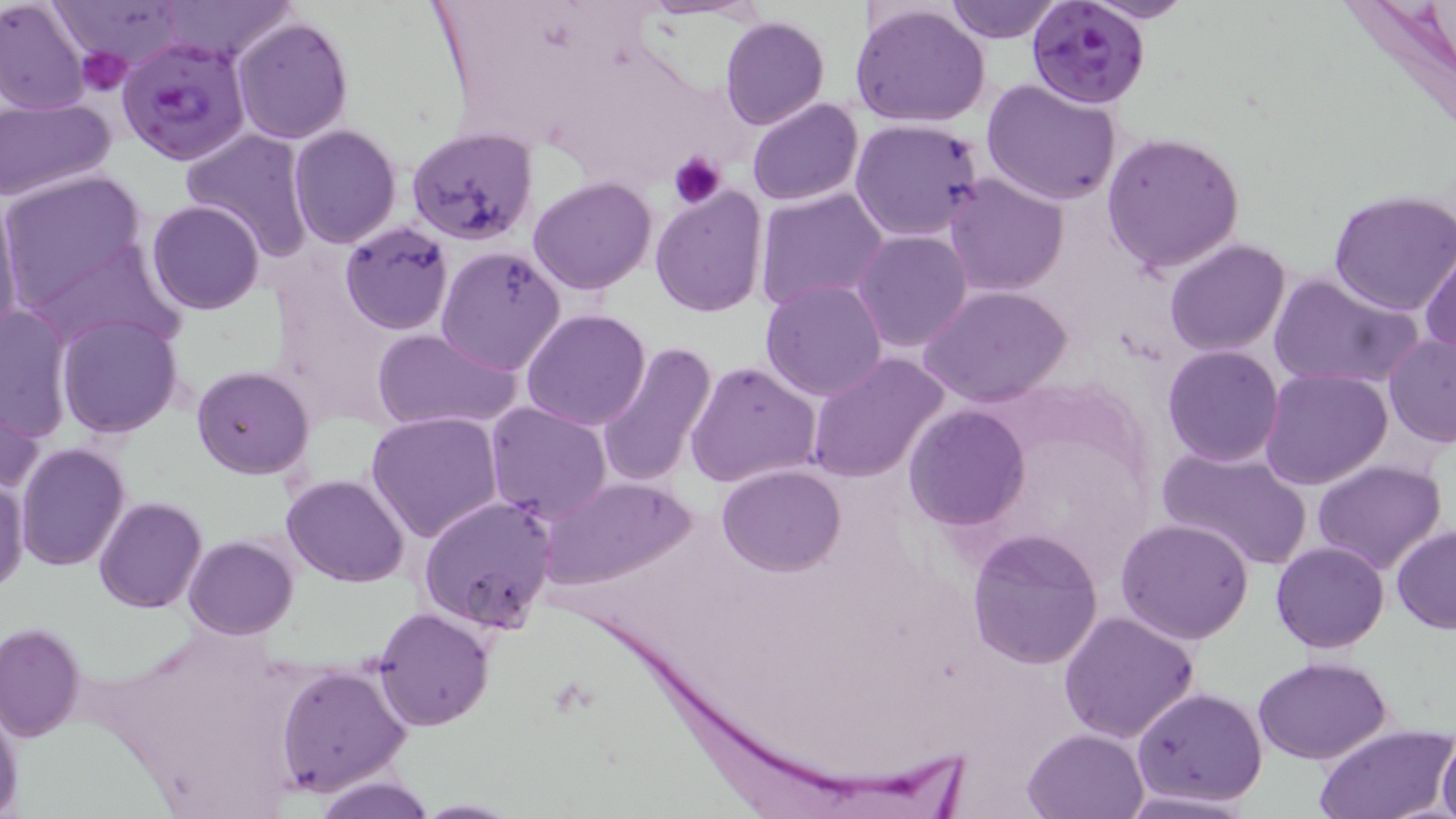
slide-level diagnosis = Plasmodium falciparum
field of view = one of a larger specimen
preparation = thin blood smear
platelet locations = approximate bounding boxes as (x1,y1)-(x2,y2) corner pairs in pixels: (77,45)-(131,94), (668,152)-(726,207)
image size = 1456×819 pixels
modality = light microscopy
Plasmodium falciparum-infected red blood cell locations = approximate bounding boxes as (x1,y1)-(x2,y2) corner pairs in pixels: (1027,0)-(1152,109), (115,37)-(252,164)
uninfected red blood cell locations = approximate bounding boxes as (x1,y1)-(x2,y2) corner pairs in pixels: (52,0)-(191,64), (157,0)-(299,65), (945,0)-(1063,43), (1085,0)-(1195,23), (0,1)-(90,116), (849,4)-(992,130), (231,15)-(353,144), (720,15)-(828,129), (981,78)-(1124,208), (0,97)-(119,203), (746,97)-(864,206), (848,117)-(986,241), (288,124)-(402,248), (405,126)-(537,247), (181,127)-(314,258), (1101,130)-(1245,274), (0,171)-(149,307), (942,173)-(1071,297), (527,177)-(657,295), (650,185)-(769,318), (753,185)-(890,312), (1327,189)-(1456,317), (0,198)-(24,345), (145,199)-(266,315), (340,220)-(454,334), (853,229)-(974,353), (27,237)-(179,350), (1164,237)-(1292,356), (435,246)-(570,376), (1419,248)-(1455,359), (1268,269)-(1426,392), (759,280)-(889,401), (918,285)-(1073,408), (0,304)-(74,450), (521,308)-(652,431), (56,313)-(184,439), (371,327)-(519,434), (1383,331)-(1456,448), (594,341)-(720,490), (1161,344)-(1286,467), (806,354)-(950,484), (684,360)-(821,489), (191,366)-(315,480), (1260,366)-(1392,490), (0,381)-(47,499), (486,401)-(612,523), (905,405)-(1030,531), (366,411)-(505,544), (16,442)-(129,571), (1158,444)-(1315,573), (1312,457)-(1446,574), (718,463)-(846,576), (1,472)-(28,597), (282,473)-(408,587), (537,476)-(698,589), (417,495)-(559,635), (94,497)-(207,614), (1116,518)-(1256,644), (1391,525)-(1456,633), (967,528)-(1103,668), (183,535)-(299,640), (1270,541)-(1391,653), (372,606)-(493,730), (1058,609)-(1202,744), (0,622)-(86,743), (1253,656)-(1391,764), (276,664)-(413,795), (1131,686)-(1269,807), (0,697)-(22,814), (1313,723)-(1453,817), (1022,727)-(1150,818), (1435,731)-(1456,818), (313,776)-(437,818), (1119,788)-(1255,818), (409,799)-(523,817)
stain = May-Grünwald-Giemsa
magnification = 1000x